Classify this cell by malaria status.
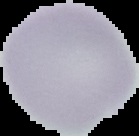
Uninfected.

Summary:
  - Preparation: thin blood smear
  - Image size: 139×136 pixels
  - Image type: segmented cell region on a black background